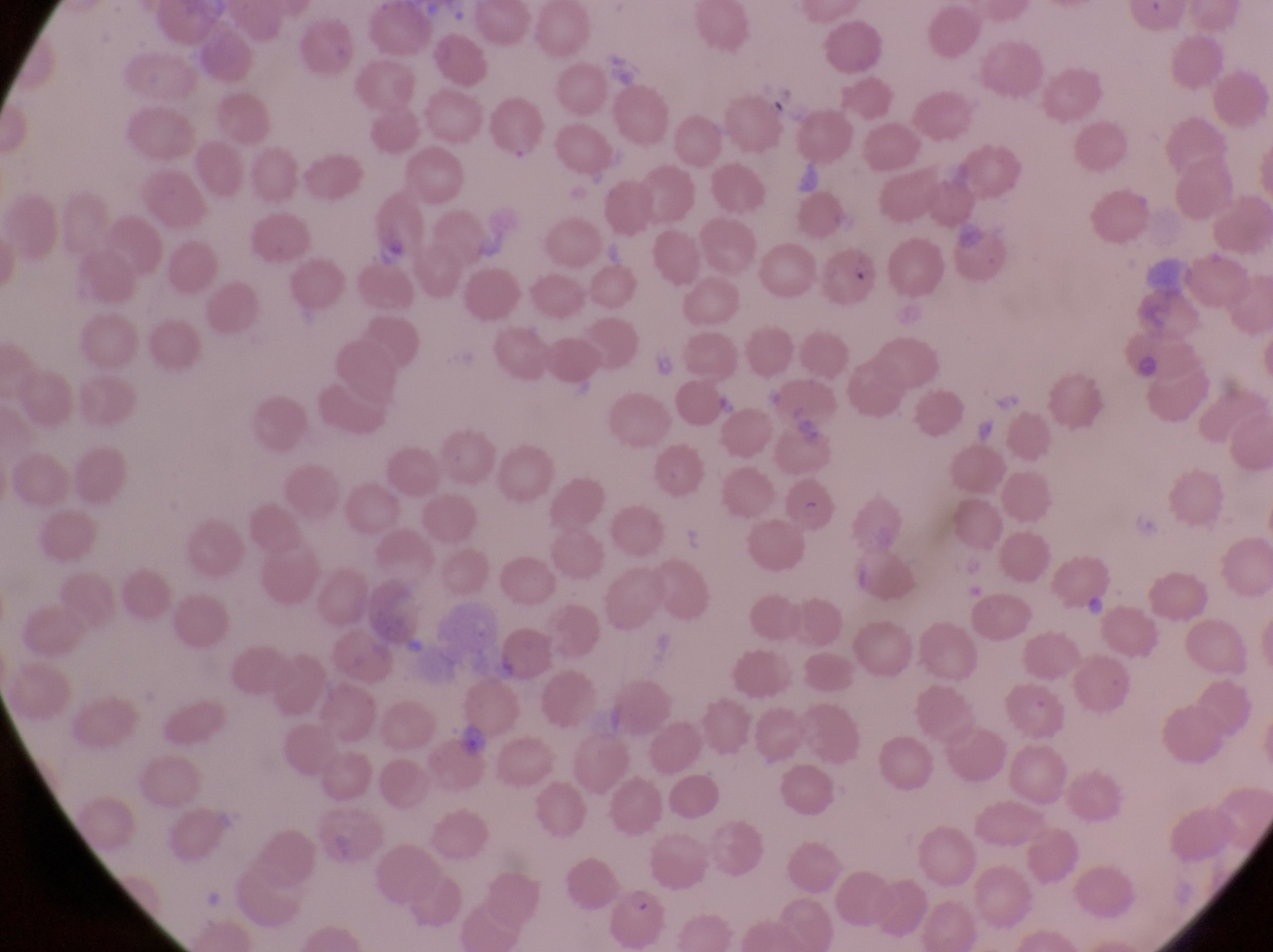

field of view = single
capture = smartphone photograph through the eyepiece of an Olympus CX-23 microscope
country = Uganda
artifact (platelet-like body, stain precipitate, or debris) locations = approximate bounding boxes as (left, top, right, bottom) in pixels: (841, 257, 869, 290)
image size = 1273×952 pixels
parasitised red blood cell locations = approximate bounding boxes as (left, top, right, bottom) in pixels: (787, 475, 844, 538), (614, 892, 679, 947)
magnification = 1000x
preparation = thin blood film